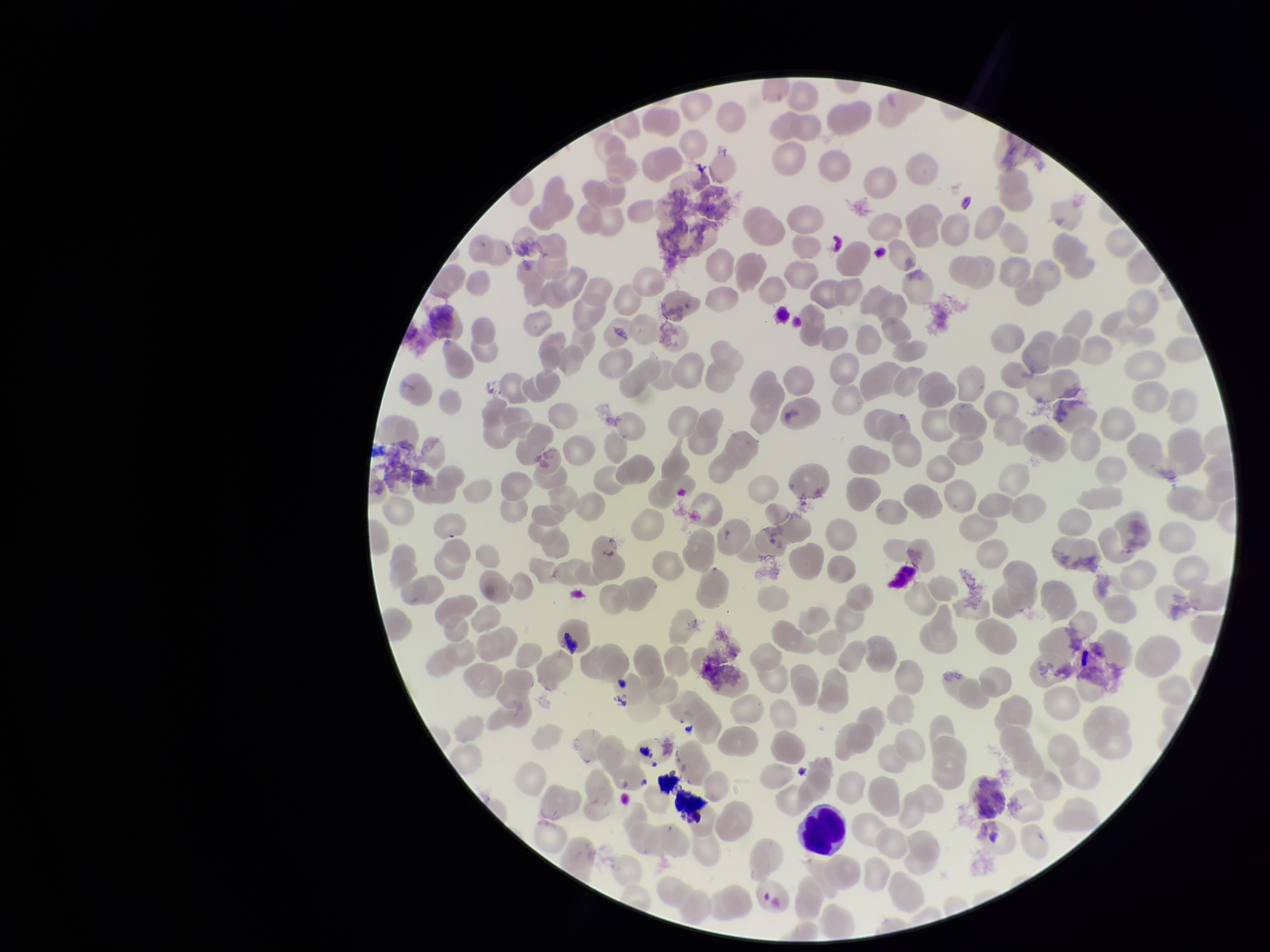

red_blood_cell_count: 250
preparation: thin
parasitized_red_blood_cells: none seen
image_size: 1270×952 pixels
stain: Giemsa
patient_malaria_status: infected
field_of_view: one from this slide
capture: smartphone photograph through the microscope eyepiece
parasitized_red_blood_cell_count: 0
species_reported_for_this_patient: Plasmodium falciparum